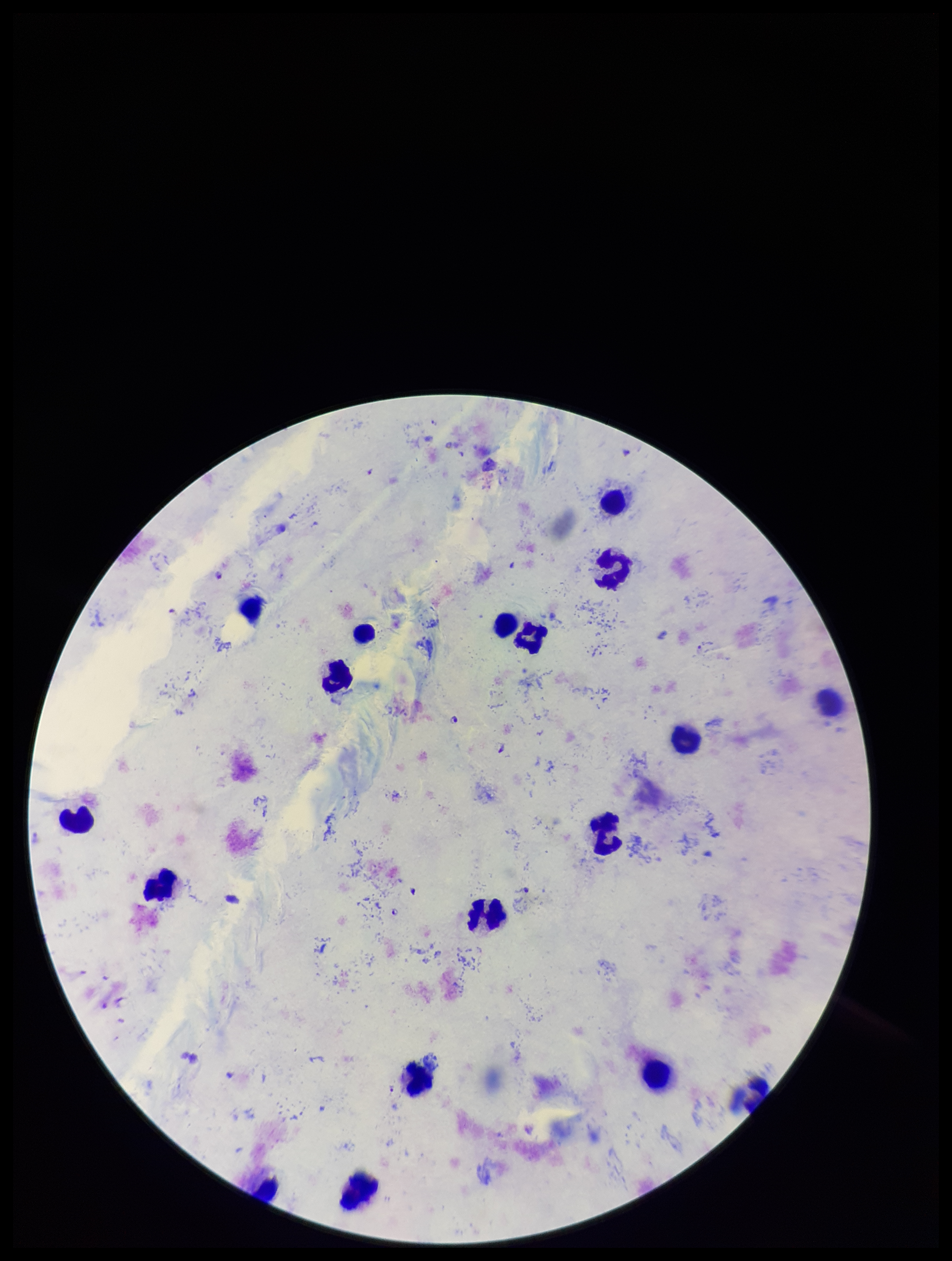
Species reported for this patient: Plasmodium falciparum. Stained with Giemsa. Plasmodium parasites: detected. Leukocyte count: 18. One field from this slide. Patient malaria status: infected. Smartphone photograph taken through the eyepiece of a microscope. Parasite count: 4. Preparation: thick blood smear. Image is 952×1261 pixels.